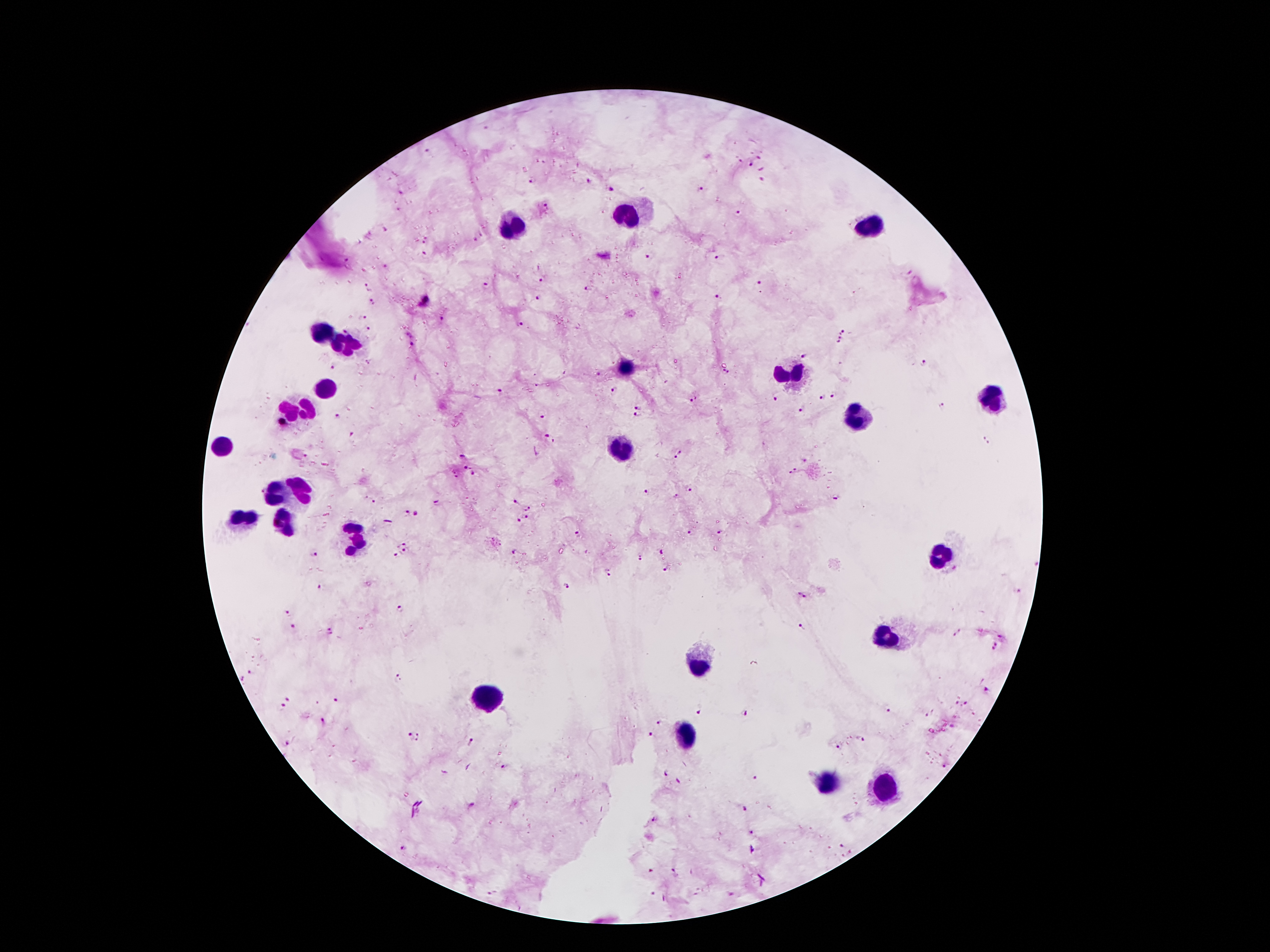
Approximate centers as (x, y) in pixels.
Summary:
  - Malaria parasite locations: (428, 152), (759, 156), (739, 161), (751, 165), (533, 179), (588, 179), (761, 180), (701, 189), (612, 190), (400, 191), (545, 204), (737, 212), (426, 239), (474, 239), (426, 255), (649, 258), (717, 259), (345, 260), (541, 279), (758, 282), (369, 286), (488, 286), (588, 288), (718, 296), (537, 297), (373, 301), (361, 316), (442, 319), (519, 324), (369, 329), (843, 332), (409, 334), (838, 341), (413, 345), (804, 357), (370, 362), (924, 363), (333, 367), (726, 371), (598, 375), (614, 389), (500, 392), (832, 395), (822, 397), (776, 398), (693, 400), (638, 406), (941, 406), (802, 409), (338, 416), (544, 416), (636, 416), (353, 434), (550, 437), (985, 439), (680, 454), (462, 456), (464, 468), (796, 470), (473, 474), (691, 490), (258, 491), (646, 492), (678, 496), (835, 497), (372, 501), (516, 502), (437, 503), (529, 509), (406, 514), (417, 514), (526, 517), (518, 521), (689, 530), (720, 531), (578, 535), (405, 543), (661, 551), (401, 552), (516, 553), (313, 554), (395, 556), (641, 557), (666, 569), (611, 572), (566, 586), (320, 587), (1019, 593), (803, 595), (399, 608), (287, 612), (293, 627), (802, 628), (331, 630), (955, 634), (1002, 635), (996, 646), (250, 671), (398, 676), (987, 689), (288, 699), (337, 700), (967, 704), (282, 707), (886, 709), (700, 710), (743, 713), (324, 720), (661, 723), (414, 737), (651, 737), (863, 741), (286, 743), (471, 743), (839, 747), (945, 767), (506, 768), (664, 773), (755, 779), (746, 809), (654, 820), (753, 833), (842, 847), (404, 849), (674, 870), (653, 872), (489, 894), (653, 894)
  - Leukocyte locations: (626, 213), (871, 223), (512, 230), (322, 335), (350, 343), (629, 368), (793, 373), (325, 392), (993, 397), (298, 408), (858, 419), (620, 445), (223, 449), (302, 488), (272, 492), (240, 521), (287, 523), (354, 537), (941, 555), (886, 639), (698, 668), (487, 699), (684, 734), (826, 781), (886, 784)
  - Capture: smartphone through the microscope eyepiece
  - Image size: 1270×952 pixels
  - Magnification: 100x
  - Stain: Giemsa
  - Field of view: one from this slide
  - Patient malaria status: infected with Plasmodium falciparum
  - Preparation: thick peripheral-blood smear